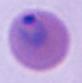
{
  "magnification": "400x or 1000x",
  "identification": "Plasmodium",
  "modality": "micrograph"
}